Classify this cell by malaria status.
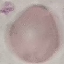

Uninfected.

Giemsa-stained preparation. Acquired by smartphone through the microscope eyepiece. Automatically extracted cell patch, resized to 64 × 64 pixels. Thin smear of blood.